Describe the morphology of the erythrocytes.
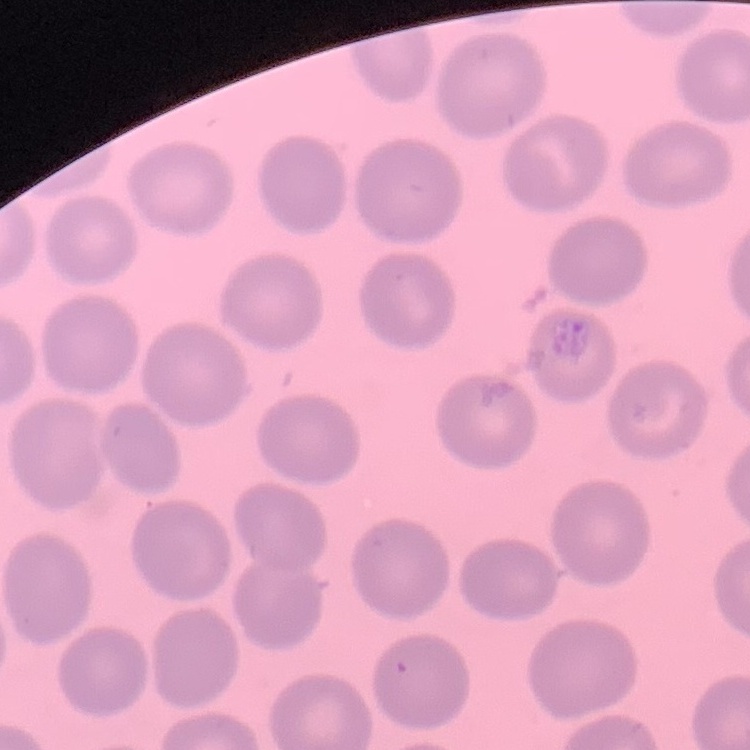

No rouleaux formation.

Thin blood smear. Stained with either Field's or Giemsa. Square crop of a larger photomicrograph.